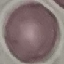
Summary:
  - Malaria status: uninfected
  - Image type: automatically extracted cell patch, resized to 64 × 64 pixels
  - Capture: smartphone through the microscope eyepiece
  - Preparation: thin smear
  - Stain: Giemsa